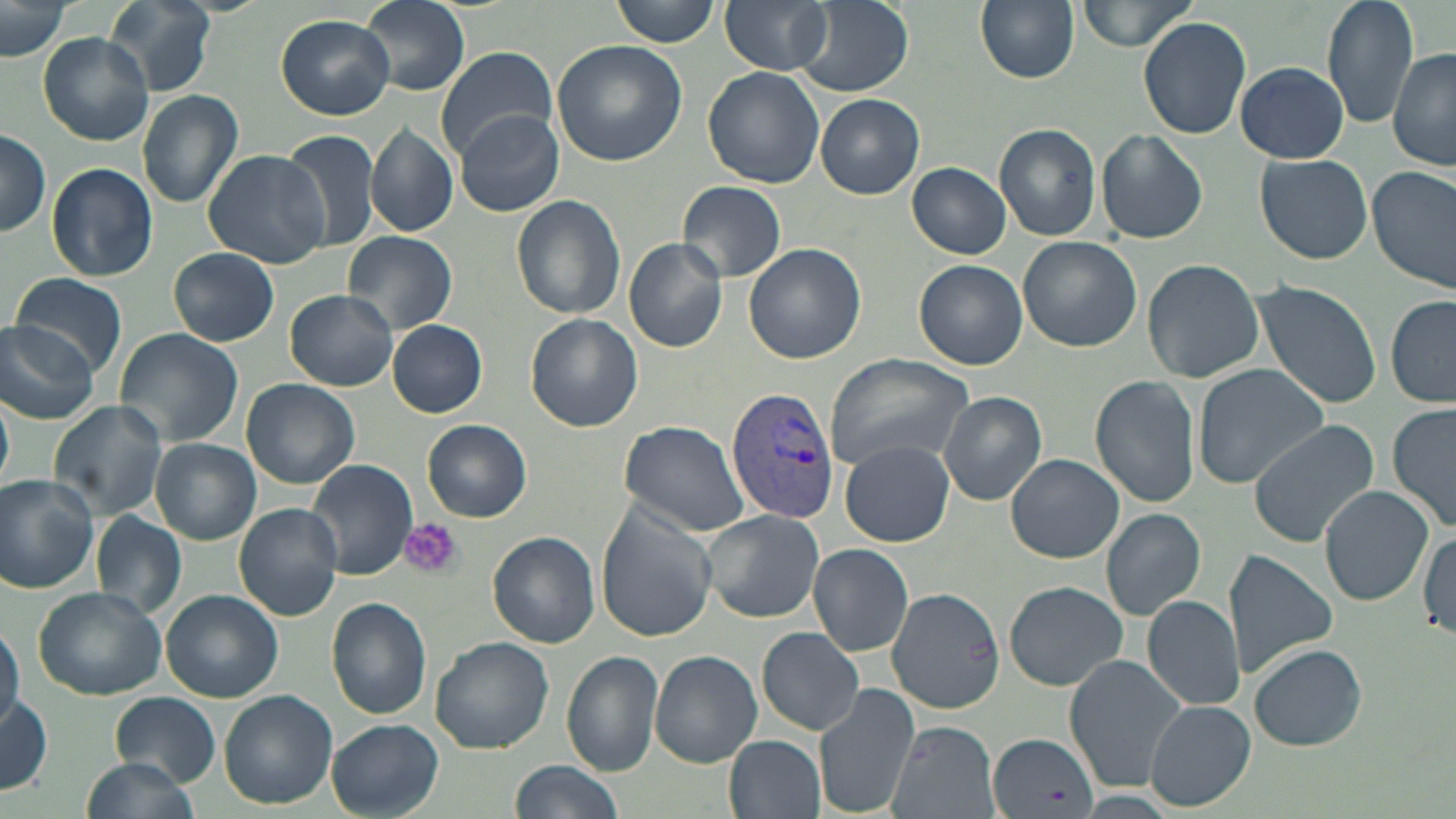
Approximate bounding boxes as (x1,y1)-(x2,y2) corner pairs in pixels. Plasmodium vivax-infected red blood cell locations: (725,386)-(840,525). Uninfected red blood cell locations: (103,0)-(215,96), (360,0)-(469,95), (613,0)-(721,48), (721,0)-(833,75), (797,0)-(914,97), (974,0)-(1080,84), (1074,0)-(1199,51), (1320,0)-(1422,128), (1,3)-(70,63), (275,14)-(395,120), (1137,17)-(1251,139), (39,33)-(154,146), (552,40)-(689,166), (435,45)-(558,159), (1388,48)-(1456,174), (1235,62)-(1350,163), (702,66)-(826,189), (137,91)-(244,207), (816,94)-(923,199), (455,110)-(564,217), (993,122)-(1103,240), (366,123)-(459,238), (278,126)-(383,251), (0,128)-(51,237), (1097,129)-(1208,243), (200,150)-(332,268), (1254,154)-(1373,265), (45,162)-(158,282), (907,162)-(1011,258), (1368,165)-(1456,296), (678,181)-(788,282), (512,194)-(627,320), (343,231)-(459,336), (1017,237)-(1142,351), (624,239)-(729,352), (743,242)-(866,364), (168,247)-(279,347), (914,258)-(1027,369), (1142,258)-(1266,385), (11,271)-(129,376), (1252,279)-(1386,410), (285,290)-(399,391), (1386,293)-(1456,409), (526,314)-(644,432), (0,319)-(101,426), (387,319)-(488,417), (113,328)-(244,447), (824,353)-(976,472), (1191,364)-(1330,488), (1090,376)-(1200,508), (242,378)-(360,489), (0,391)-(14,490), (938,392)-(1048,505), (46,400)-(171,521), (1387,404)-(1455,536), (423,419)-(532,523), (617,420)-(750,538), (1245,420)-(1380,548), (151,439)-(261,545), (841,440)-(955,547), (1005,453)-(1124,564), (303,459)-(418,581), (0,473)-(100,594), (1318,486)-(1432,607), (233,503)-(343,622), (597,504)-(719,641), (699,509)-(826,623), (1100,509)-(1206,621), (91,511)-(185,620), (1418,530)-(1456,643), (487,531)-(601,649), (807,543)-(914,658), (1225,549)-(1339,682), (1003,580)-(1129,691), (32,584)-(171,699), (886,585)-(1006,717), (162,589)-(284,703), (1140,595)-(1245,713), (327,598)-(432,719), (0,621)-(22,733), (758,627)-(865,737), (430,637)-(555,755), (1247,644)-(1366,750), (562,649)-(663,777), (649,649)-(762,768), (1062,656)-(1191,793), (813,682)-(920,817), (221,691)-(336,806), (109,693)-(221,784), (0,694)-(52,797), (1146,700)-(1255,811), (327,720)-(443,816), (887,722)-(999,819), (990,731)-(1098,817), (724,732)-(825,819), (81,757)-(199,817), (507,760)-(622,819). Platelet locations: (399,518)-(461,580). Slide-level diagnosis: Plasmodium vivax. 1000x magnification. Thin blood film. Image is 1456×819 pixels. Light microscopy. One field of a larger specimen. May-Grünwald-Giemsa-stained preparation.